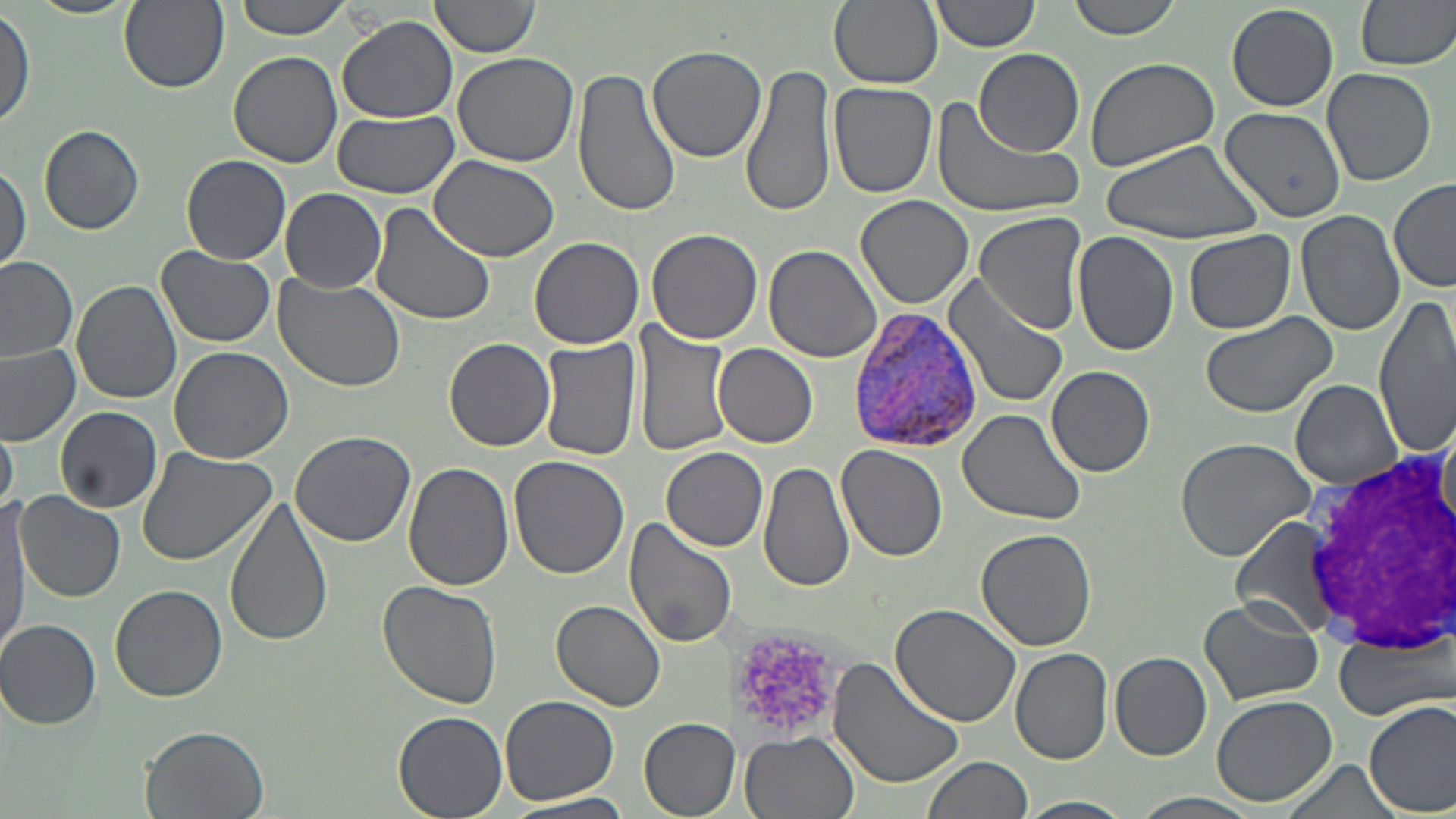
Summary:
  - Coordinate format: approximate bounding boxes as (x1, y1, x2, y2) in pixels
  - White blood cell locations: (1301, 441, 1452, 655)
  - Plasmodium vivax-infected red blood cell locations: (845, 307, 986, 453)
  - Uninfected red blood cell locations: (25, 0, 141, 19), (119, 0, 228, 92), (232, 0, 356, 41), (829, 0, 942, 90), (929, 0, 1042, 53), (1065, 0, 1182, 40), (1355, 0, 1456, 73), (427, 1, 540, 61), (1227, 4, 1337, 111), (0, 7, 35, 128), (337, 16, 458, 124), (645, 43, 766, 166), (974, 49, 1084, 158), (229, 51, 343, 168), (451, 53, 577, 167), (1085, 57, 1219, 174), (740, 63, 837, 220), (571, 66, 683, 222), (1321, 67, 1437, 187), (827, 83, 938, 200), (928, 96, 1088, 222), (1220, 106, 1347, 222), (327, 110, 460, 197), (39, 125, 145, 236), (1098, 137, 1265, 245), (182, 155, 291, 265), (431, 155, 558, 262), (0, 161, 29, 271), (1389, 179, 1456, 292), (280, 187, 386, 293), (856, 195, 974, 309), (368, 201, 496, 328), (1296, 210, 1406, 336), (972, 211, 1087, 333), (645, 229, 763, 345), (1184, 230, 1295, 334), (1071, 231, 1178, 356), (529, 237, 645, 350), (764, 244, 882, 362), (155, 246, 277, 347), (0, 256, 78, 362), (942, 270, 1069, 410), (271, 271, 406, 392), (73, 279, 186, 403), (1374, 293, 1456, 458), (1197, 311, 1339, 419), (633, 323, 732, 459), (445, 337, 556, 453), (537, 337, 643, 462), (0, 344, 81, 443), (713, 344, 819, 449), (169, 346, 293, 464), (1046, 365, 1157, 477), (1290, 380, 1404, 489), (56, 406, 164, 512), (957, 409, 1086, 526), (0, 423, 17, 518), (290, 429, 416, 547), (1174, 435, 1318, 563), (137, 445, 278, 566), (836, 445, 949, 563), (661, 447, 768, 551), (508, 456, 630, 578), (758, 460, 856, 594), (405, 463, 515, 590), (15, 492, 126, 602), (226, 498, 333, 650), (0, 504, 32, 650), (623, 517, 739, 649), (1230, 517, 1348, 638), (975, 529, 1096, 650), (377, 580, 504, 709), (111, 582, 227, 701), (1199, 596, 1323, 707), (552, 599, 667, 711), (890, 604, 1023, 729), (1, 619, 101, 728), (1335, 635, 1451, 721), (1010, 648, 1114, 766), (1110, 652, 1212, 760), (828, 657, 966, 790), (1210, 693, 1337, 807), (499, 695, 619, 804), (1365, 700, 1456, 816), (392, 711, 508, 819), (638, 717, 739, 817), (140, 725, 270, 819), (740, 731, 860, 819), (923, 756, 1032, 819), (1279, 759, 1404, 819), (1130, 791, 1264, 819), (506, 795, 633, 819), (1021, 796, 1131, 819)
  - Platelet locations: (731, 628, 839, 732)
  - Slide-level diagnosis: Plasmodium vivax
  - Image size: 1456×819 pixels
  - Field of view: single
  - Magnification: 1000x
  - Preparation: thin blood film
  - Modality: light microscopy
  - Stain: May-Grünwald-Giemsa